Classify this cell by malaria status.
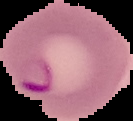

It is parasitized.

image type = segmented cell region with the area outside set to black
image size = 133×121 pixels
preparation = thin blood film